Assess this cell for malaria.
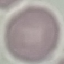
Uninfected.

capture = smartphone through the microscope eyepiece
preparation = thin blood film
image type = automatically extracted cell patch, resized to 64 × 64 pixels
stain = Giemsa